Assess for parasitized red blood cells.
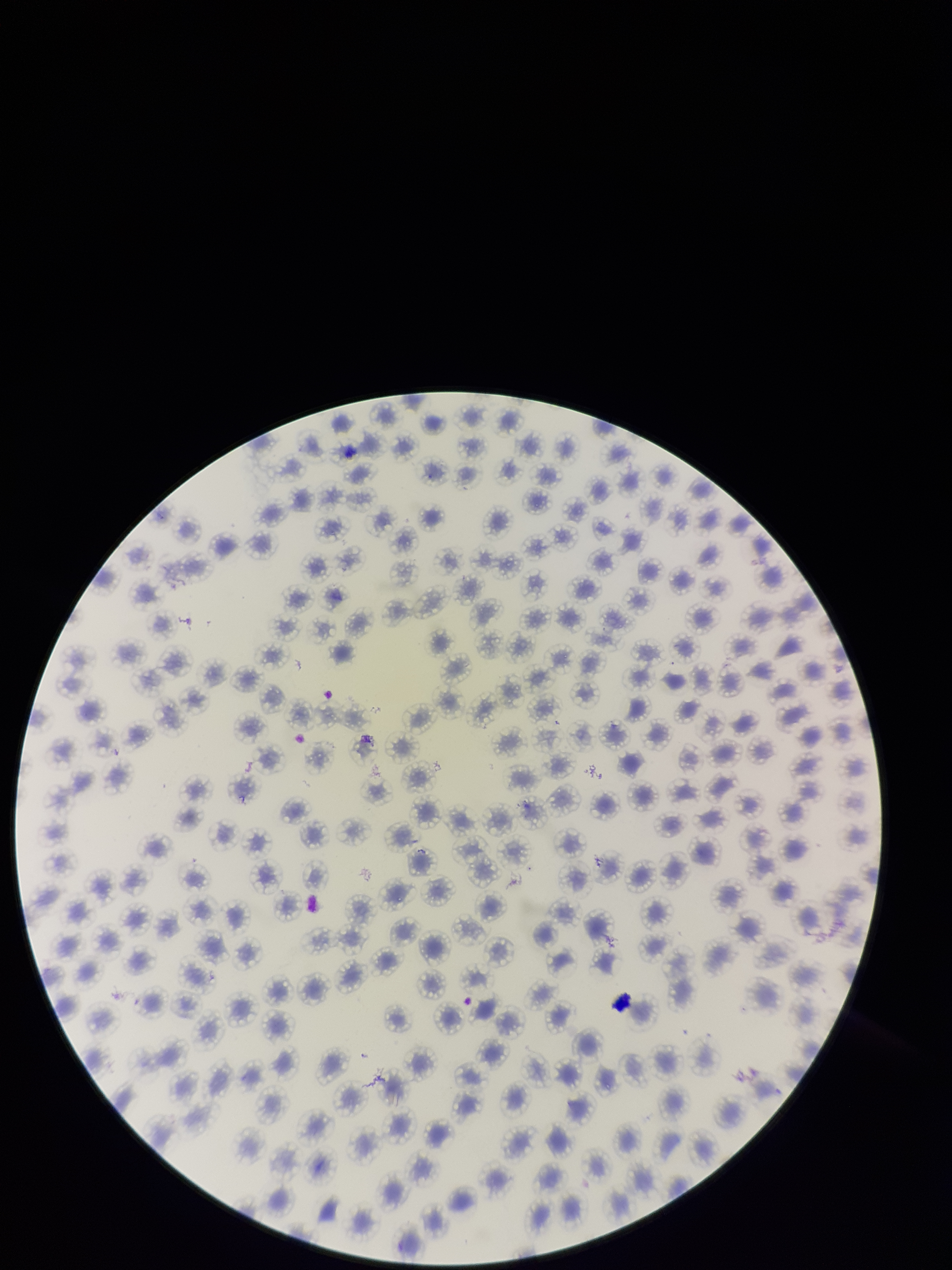

None seen.

Summary:
  - Stain: Giemsa
  - Red blood cell count: 125
  - Field of view: single
  - Capture: smartphone photograph through the microscope eyepiece
  - Patient malaria status: positive
  - Image size: 952×1270 pixels
  - Preparation: thin
  - Parasitized red blood cell count: 0
  - Species reported for this patient: Plasmodium falciparum